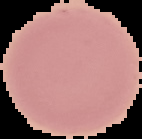
From a thin blood film. Malaria status: uninfected. The area outside the segmented cell region is set to black. Image is 142×139 pixels.